Assess this cell for malaria.
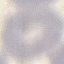
It is uninfected.

Automatically extracted cell patch, resized to 64 × 64 pixels. Giemsa-stained preparation. Acquired by smartphone through the microscope eyepiece. Thin blood film.